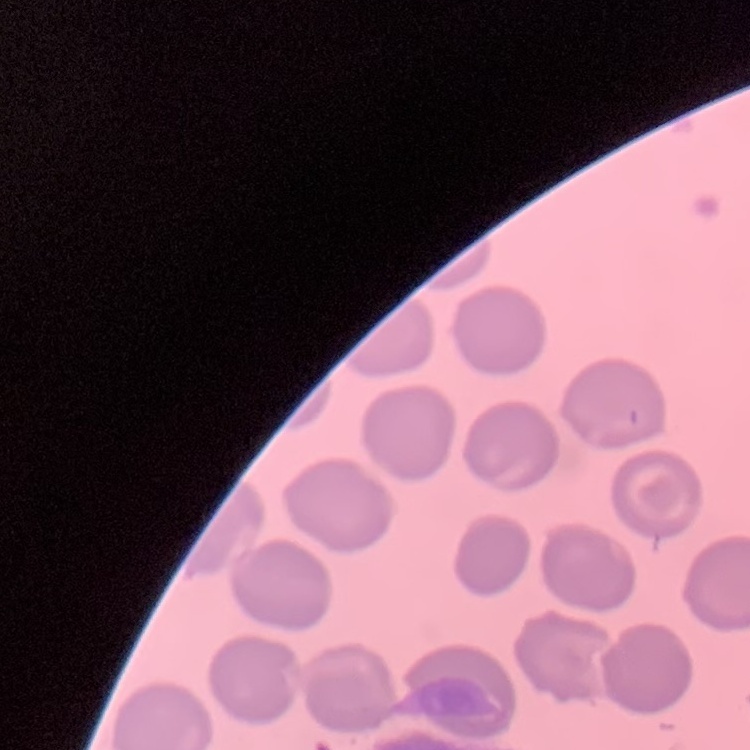
{
  "red_blood_cell_morphology": "no rouleaux formation",
  "stain": "Field's or Giemsa",
  "preparation": "thin peripheral smear",
  "image_type": "square crop of a larger photomicrograph"
}